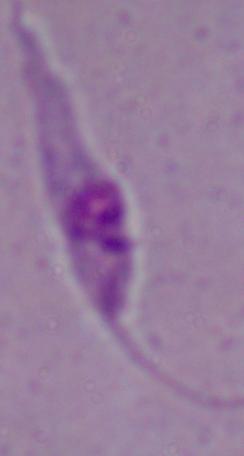 A Leishmania parasite is seen. Micrograph. Captured at 1000x magnification.